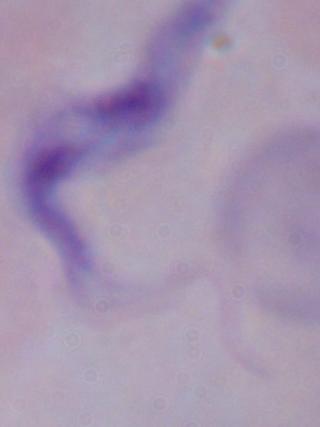

magnification = 1000x
identification = trypanosome
modality = photomicrograph